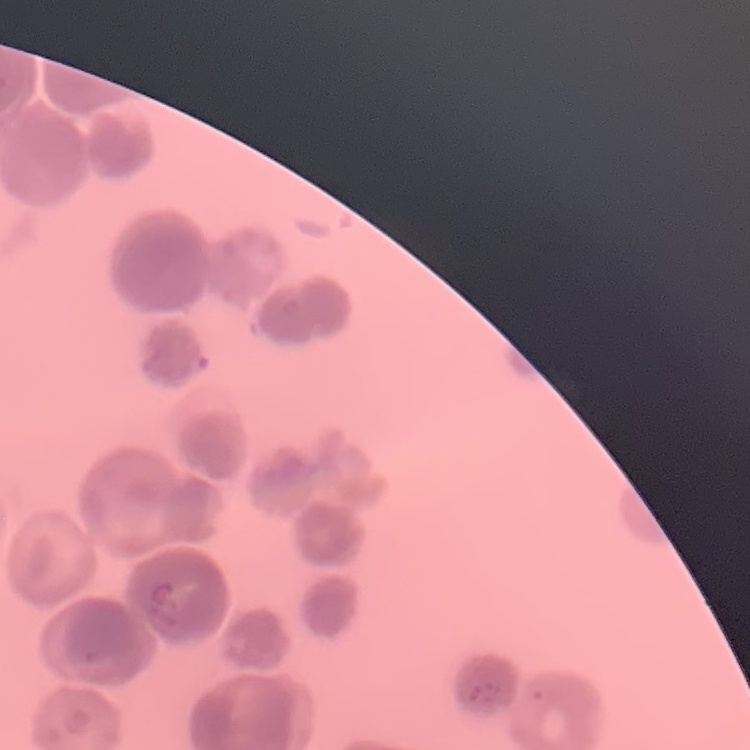
red_blood_cell_morphology: rouleaux formation
image_type: one tile cut from a larger photomicrograph
stain: Field's or Giemsa
preparation: thin blood smear